Identify the parasite.
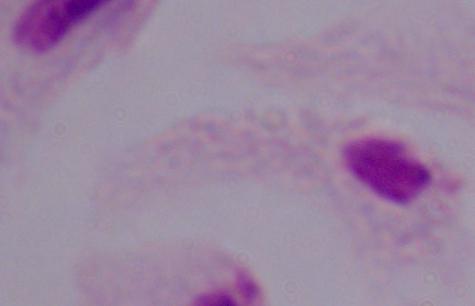

This is a trichomonad.

magnification = 1000x
modality = micrograph